Name the parasite shown.
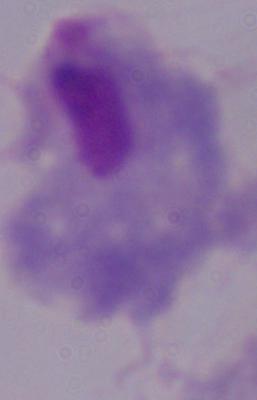

This is a trichomonad.

1000x magnification. Micrograph.